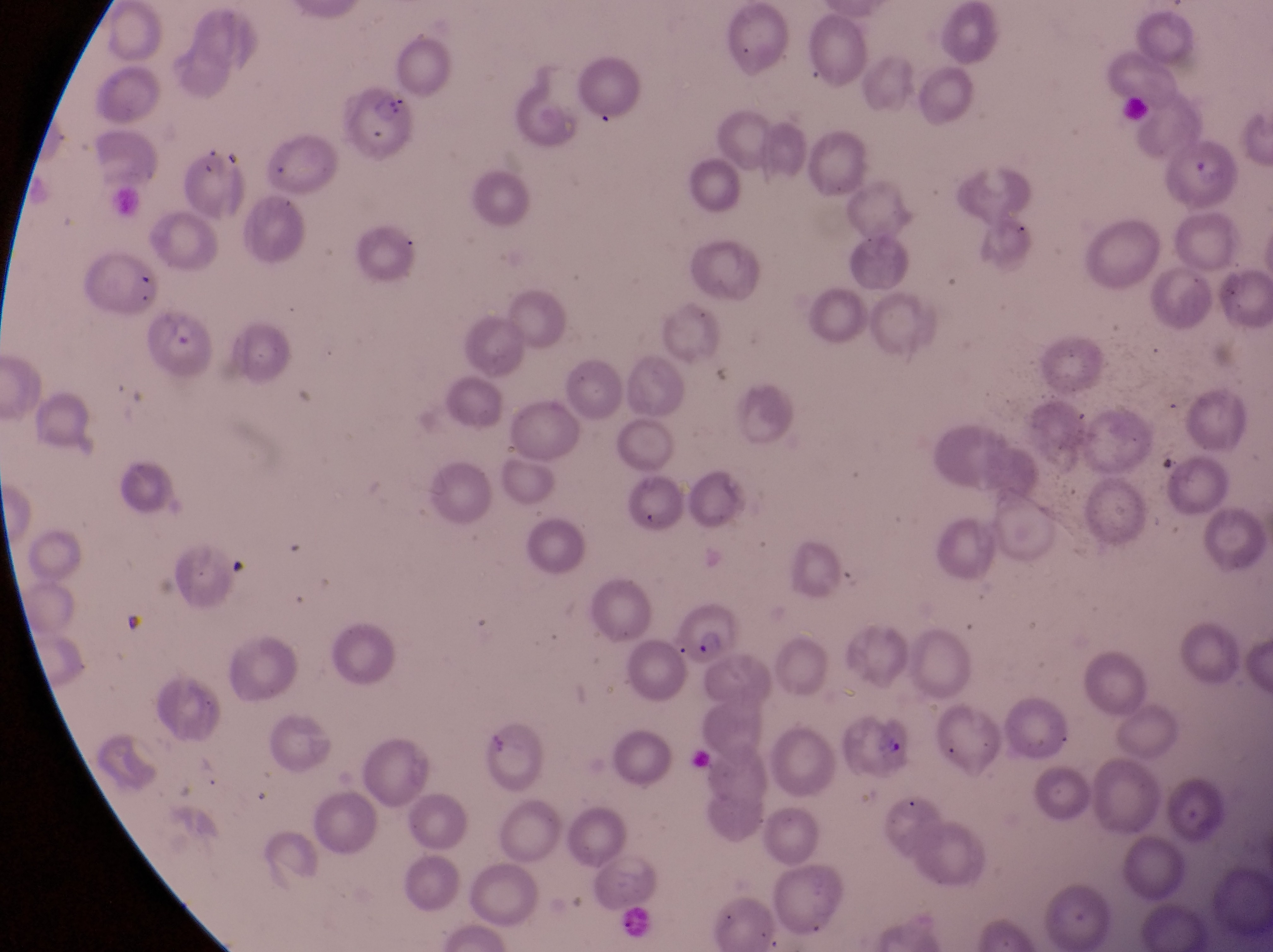

capture = smartphone photograph through the eyepiece of an Olympus CX-23 microscope
parasitised red blood cell locations = approximate bounding boxes as left top right bottom in pixels: 350 80 422 163; 1173 139 1242 216; 170 148 244 220; 147 307 221 382; 686 592 744 662; 834 704 926 782
country = Uganda
magnification = 1000x
field of view = single
preparation = thin blood film
image size = 1273×952 pixels